Report the malaria status of this cell.
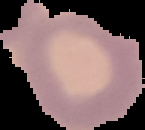

Uninfected.

Summary:
  - Image size: 145×130 pixels
  - Preparation: thin blood film
  - Image type: cell region segmented out of the field of view; surrounding area masked to black